Outline each blood parasite and name the species.
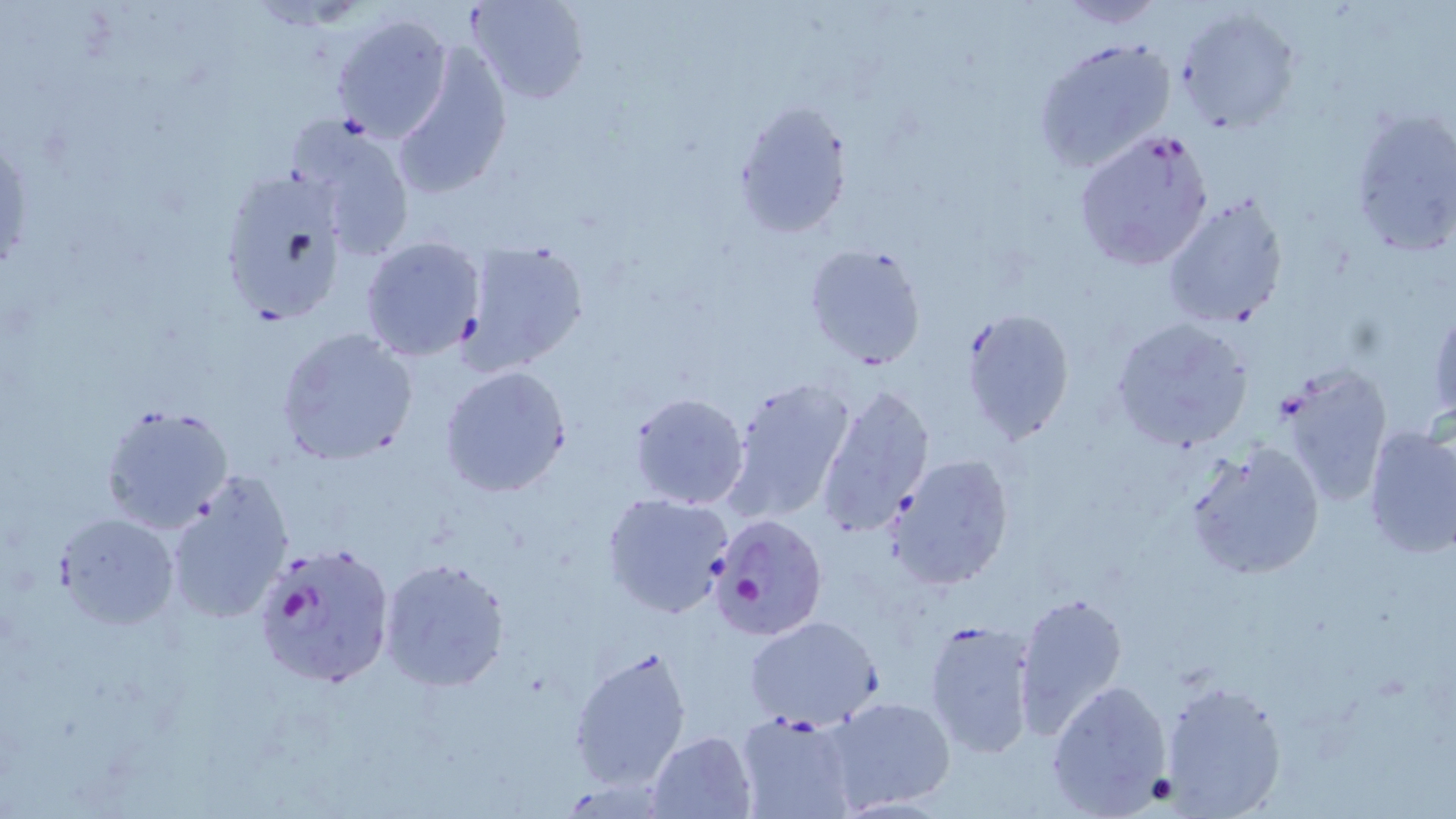

Approximate bounding boxes as (x1,y1)-(x2,y2) corner pairs in pixels.
Plasmodium falciparum-infected red blood cells: (1072,128)-(1214,274), (707,511)-(828,641), (250,539)-(396,693).
No Plasmodium ovale, Plasmodium malariae, Plasmodium vivax, Babesia divergens, or Trypanosoma brucei observed.

Summary:
  - Uninfected red blood cell locations: (467,0)-(589,106), (1053,1)-(1167,28), (1175,6)-(1300,135), (329,11)-(454,144), (1032,35)-(1178,173), (389,43)-(514,199), (731,99)-(850,240), (1348,104)-(1456,263), (287,112)-(419,260), (216,173)-(344,326), (1163,194)-(1290,329), (359,236)-(488,361), (456,239)-(591,373), (804,242)-(928,370), (1427,306)-(1456,425), (958,308)-(1076,445), (1108,318)-(1254,455), (276,328)-(418,465), (438,365)-(572,498), (1274,365)-(1393,509), (723,377)-(857,525), (813,380)-(935,539), (626,392)-(751,511), (100,403)-(231,533), (1362,424)-(1456,559), (1184,439)-(1326,580), (886,453)-(1015,590), (163,471)-(295,626), (601,491)-(736,618), (55,513)-(180,628), (379,555)-(510,691), (1014,591)-(1128,735), (744,615)-(883,731), (922,617)-(1039,763), (567,643)-(695,794), (1046,677)-(1173,815), (1158,679)-(1284,816), (823,694)-(957,813), (735,711)-(858,819), (646,729)-(759,818)
  - Slide-level diagnosis: Plasmodium falciparum
  - Field of view: one of a larger specimen
  - Magnification: 1000x
  - Image size: 1456×819 pixels
  - Stain: May-Grünwald-Giemsa
  - Preparation: thin blood smear
  - Modality: light microscopy